Identify the cell.
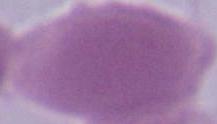
This is an erythrocyte.

Summary:
  - Magnification: 1000x
  - Modality: micrograph